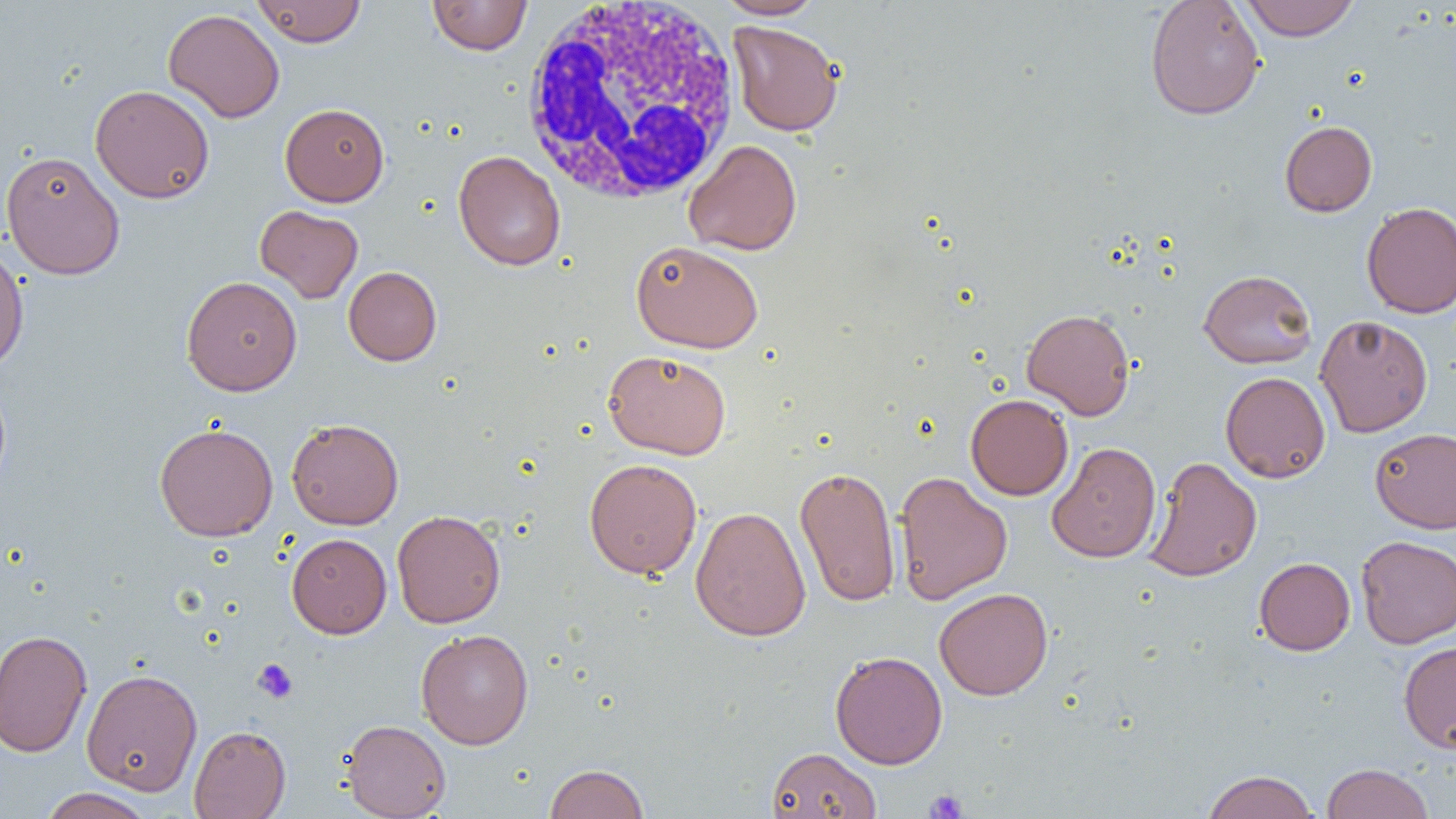
Approximate bounding boxes as (x1, y1, x2, y2) in pixels. White blood cell locations: (518, 0, 745, 207). Uninfected red blood cell locations: (251, 0, 366, 46), (427, 0, 532, 55), (716, 0, 825, 20), (1239, 0, 1360, 40), (1145, 1, 1265, 120), (162, 8, 285, 123), (728, 20, 844, 136), (90, 84, 215, 203), (280, 103, 389, 206), (1279, 120, 1377, 217), (683, 139, 802, 256), (1, 150, 125, 279), (453, 150, 566, 271), (1361, 201, 1456, 318), (255, 205, 363, 303), (631, 240, 763, 353), (0, 244, 29, 374), (343, 266, 442, 365), (1198, 269, 1317, 368), (1209, 269, 1321, 480), (180, 275, 302, 396), (1021, 308, 1135, 420), (1315, 315, 1433, 437), (603, 350, 732, 459), (1220, 371, 1331, 483), (965, 394, 1073, 500), (286, 418, 404, 529), (154, 422, 278, 541), (1370, 428, 1456, 533), (1046, 442, 1161, 563), (1144, 456, 1263, 582), (583, 458, 702, 579), (794, 464, 901, 608), (893, 471, 1012, 605), (690, 506, 811, 642), (392, 510, 505, 628), (287, 533, 391, 638), (1355, 535, 1456, 648), (1254, 557, 1355, 655), (934, 587, 1053, 700), (0, 628, 93, 758), (416, 628, 534, 750), (1398, 641, 1456, 753), (829, 650, 947, 769), (81, 667, 203, 796), (341, 719, 451, 818), (189, 725, 290, 818), (767, 747, 881, 819), (1321, 762, 1434, 819), (544, 763, 649, 819), (1201, 770, 1320, 819), (38, 787, 154, 819). Platelet locations: (252, 659, 297, 703), (924, 789, 968, 818). Slide-level diagnosis: negative for blood parasites. Image is 1456×819 pixels. One field of a larger specimen. Optical microscopy. Thin blood smear. 1000x magnification.